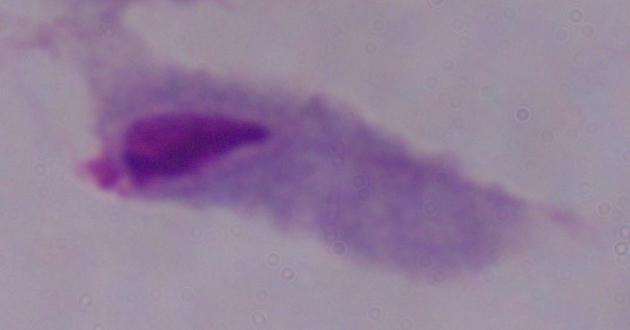
identification: trichomonad
modality: micrograph
magnification: 1000x